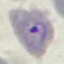
result = malaria parasites detected
capture = smartphone camera at the microscope eyepiece
stain = Giemsa
preparation = thin smear
image type = cell patch, automatically extracted from a larger field of view and resized to 64 × 64 pixels